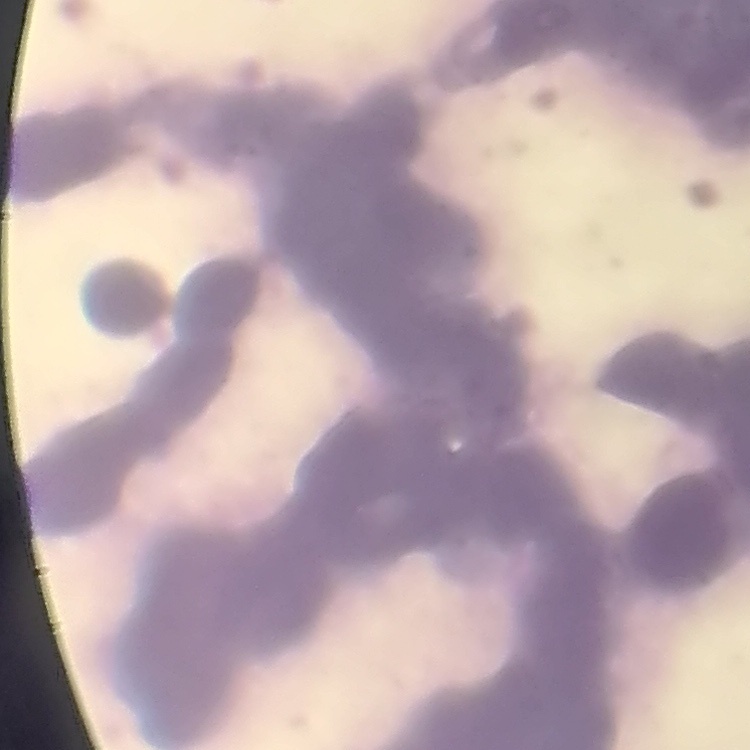

Summary:
  - Red blood cell morphology: rouleaux formation
  - Stain: Field's or Giemsa
  - Image type: one tile cut from a larger photomicrograph
  - Preparation: thin peripheral smear